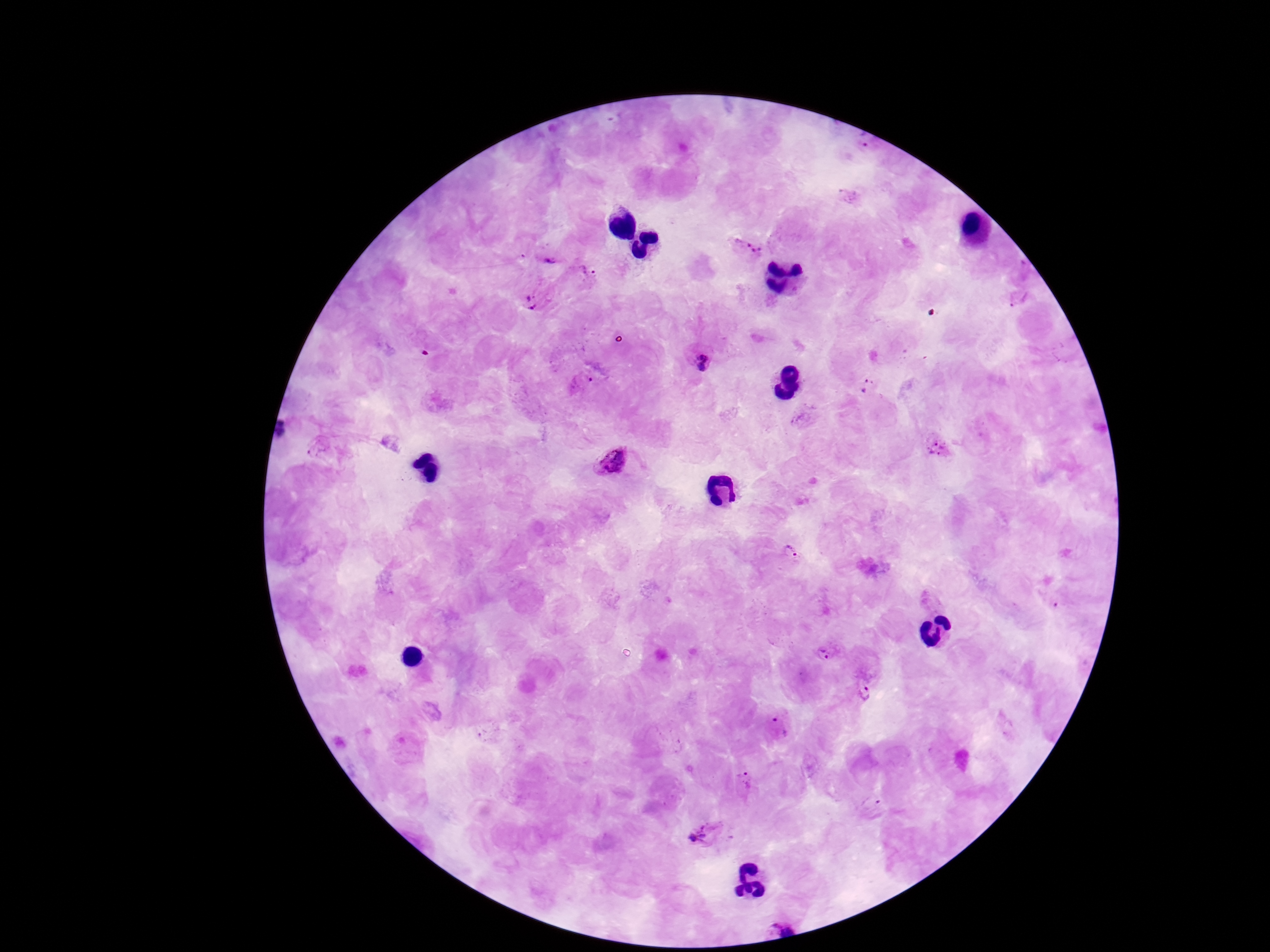
field of view = one from this slide
stain = Giemsa
image size = 1270×952 pixels
magnification = 100x
preparation = thick blood smear
Plasmodium parasite locations = approximate centers as {x, y} in pixels: {746, 243}, {548, 249}, {587, 268}, {532, 300}, {697, 358}, {583, 381}, {867, 385}, {937, 448}, {610, 462}, {786, 557}, {828, 653}, {866, 691}, {779, 726}, {743, 786}, {871, 804}, {707, 834}
capture = smartphone camera through the microscope eyepiece
patient malaria status = infected